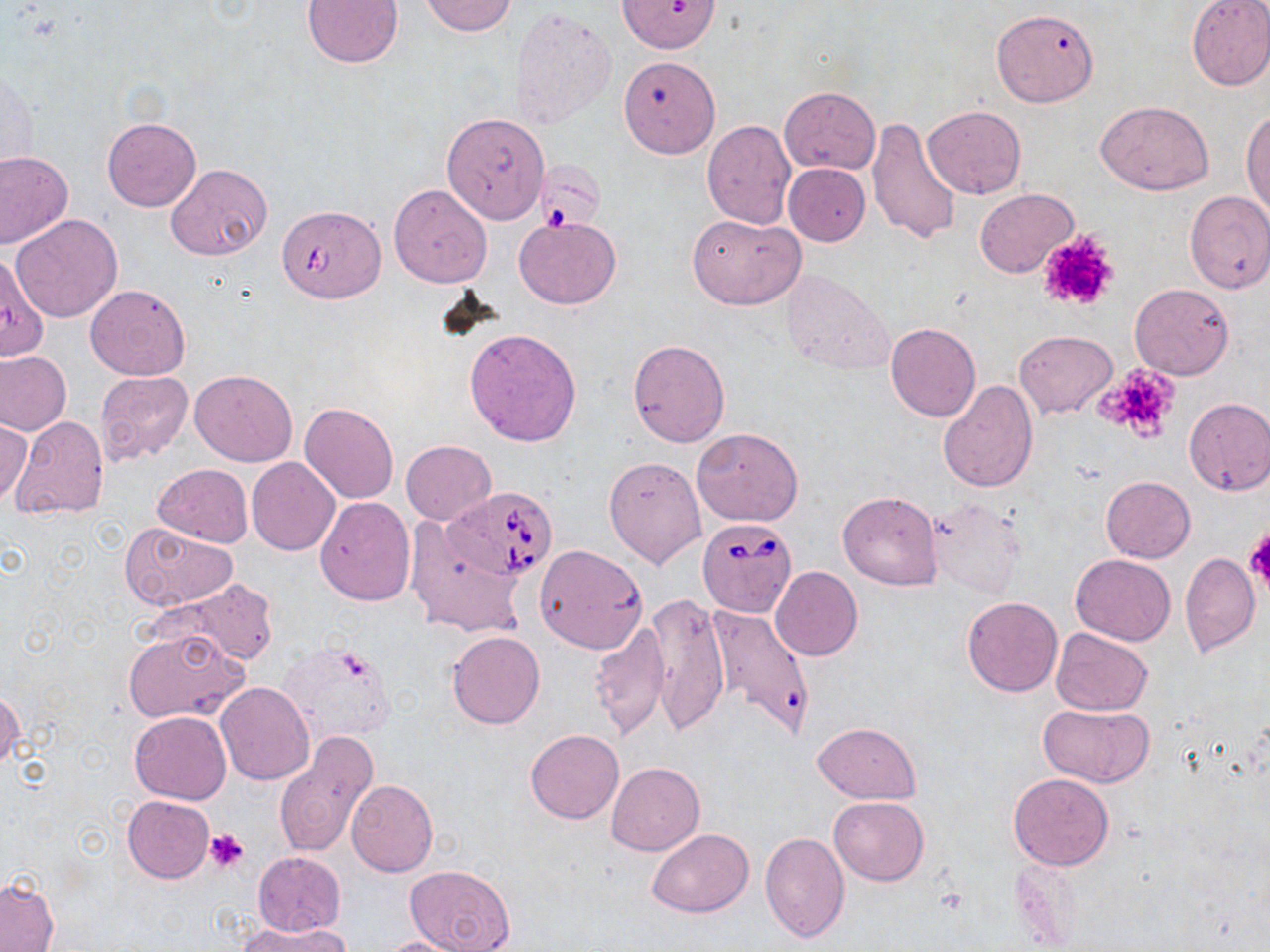
Approximate bounding boxes as (x1, y1, x2, y2) in pixels. Uninfected red blood cell locations: (302, 0, 403, 69), (616, 0, 721, 53), (1185, 0, 1270, 91), (420, 1, 518, 36), (509, 7, 616, 131), (991, 8, 1099, 107), (618, 56, 720, 158), (3, 64, 39, 176), (780, 86, 880, 175), (1096, 100, 1212, 195), (923, 105, 1026, 200), (1242, 107, 1270, 218), (441, 111, 551, 225), (102, 116, 202, 212), (866, 118, 962, 245), (702, 120, 796, 229), (0, 150, 72, 248), (533, 159, 604, 229), (165, 163, 271, 261), (784, 163, 870, 245), (388, 183, 492, 288), (975, 187, 1078, 279), (1183, 190, 1270, 293), (282, 209, 388, 305), (689, 212, 804, 309), (11, 213, 122, 322), (513, 216, 621, 309), (0, 249, 52, 365), (780, 268, 895, 378), (1129, 283, 1234, 380), (84, 284, 190, 380), (885, 323, 980, 422), (465, 328, 581, 447), (1015, 330, 1118, 419), (627, 338, 730, 447), (0, 351, 71, 434), (190, 368, 297, 466), (95, 370, 193, 463), (938, 378, 1039, 494), (1184, 397, 1270, 496), (299, 402, 398, 503), (0, 415, 34, 509), (11, 415, 108, 520), (691, 426, 804, 527), (401, 439, 496, 525), (604, 456, 706, 569), (246, 457, 340, 555), (152, 463, 252, 547), (1100, 476, 1195, 563), (837, 490, 943, 590), (316, 496, 416, 606), (925, 497, 1025, 596), (405, 519, 530, 639), (120, 523, 238, 610), (535, 544, 648, 653), (1179, 552, 1260, 658), (1070, 554, 1176, 644), (771, 566, 863, 661), (163, 579, 279, 665), (647, 593, 730, 735), (962, 596, 1063, 696), (703, 604, 815, 740), (588, 619, 669, 741), (123, 628, 247, 724), (1050, 628, 1154, 716), (447, 631, 544, 729), (279, 639, 399, 746), (214, 682, 315, 786), (0, 688, 23, 771), (1023, 702, 1139, 864), (1039, 703, 1154, 788), (130, 711, 232, 804), (811, 721, 921, 803), (526, 728, 623, 822), (272, 731, 378, 859), (606, 762, 704, 856), (1007, 773, 1114, 870), (345, 779, 438, 876), (123, 795, 215, 883), (828, 796, 928, 885), (648, 828, 753, 917), (760, 831, 849, 943), (252, 851, 345, 936), (406, 864, 515, 952), (0, 877, 57, 952), (239, 921, 349, 952), (378, 935, 478, 952). Platelet locations: (1037, 230, 1119, 313), (1093, 362, 1183, 443), (1244, 529, 1270, 590), (204, 829, 250, 872). Babesia divergens-infected red blood cell locations: (449, 485, 557, 580), (698, 516, 797, 617). Slide-level diagnosis: Babesia divergens. 1000x magnification. Optical microscopy. Thin blood smear. Single field of view. Image is 1270×952 pixels. May-Grünwald-Giemsa stain.